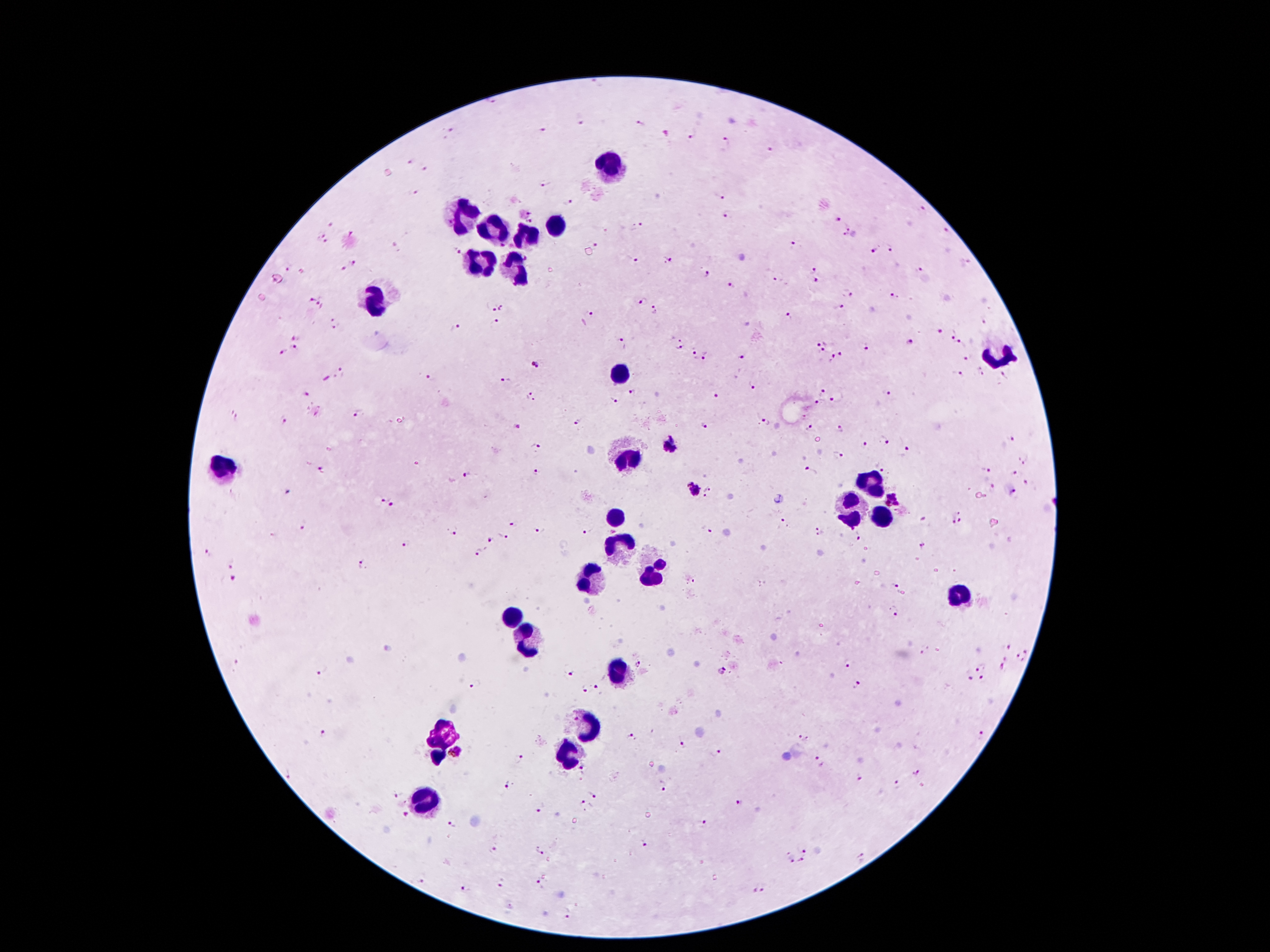

{
  "leukocyte_locations": "approximate object centers, in pixels from the top-left corner: (x=609, y=163), (x=465, y=215), (x=559, y=226), (x=493, y=229), (x=527, y=236), (x=478, y=263), (x=515, y=271), (x=375, y=292), (x=998, y=357), (x=619, y=375), (x=627, y=457), (x=223, y=466), (x=871, y=483), (x=854, y=509), (x=878, y=514), (x=615, y=521), (x=620, y=544), (x=649, y=573), (x=591, y=577), (x=962, y=593), (x=512, y=616), (x=522, y=636), (x=619, y=676), (x=587, y=726), (x=441, y=732), (x=573, y=752), (x=436, y=756), (x=425, y=805)",
  "malaria_parasite_locations": "approximate object centers, in pixels from the top-left corner: (x=492, y=102), (x=579, y=118), (x=641, y=124), (x=450, y=130), (x=541, y=132), (x=690, y=133), (x=723, y=143), (x=771, y=152), (x=410, y=162), (x=425, y=167), (x=546, y=183), (x=414, y=193), (x=720, y=195), (x=568, y=203), (x=923, y=209), (x=531, y=212), (x=727, y=213), (x=837, y=218), (x=531, y=220), (x=330, y=224), (x=637, y=226), (x=849, y=226), (x=321, y=231), (x=946, y=231), (x=351, y=233), (x=845, y=237), (x=596, y=245), (x=792, y=245), (x=326, y=246), (x=502, y=246), (x=890, y=248), (x=874, y=250), (x=458, y=251), (x=526, y=258), (x=633, y=260), (x=668, y=261), (x=353, y=263), (x=969, y=263), (x=286, y=268), (x=341, y=270), (x=812, y=270), (x=918, y=270), (x=301, y=272), (x=708, y=274), (x=778, y=279), (x=817, y=280), (x=731, y=287), (x=848, y=294), (x=894, y=296), (x=321, y=299), (x=312, y=300), (x=643, y=300), (x=837, y=307), (x=491, y=309), (x=503, y=309), (x=655, y=311), (x=592, y=315), (x=789, y=316), (x=336, y=319), (x=984, y=322), (x=495, y=324), (x=336, y=329), (x=455, y=329), (x=939, y=330), (x=954, y=334), (x=296, y=336), (x=682, y=339), (x=621, y=343), (x=817, y=344), (x=909, y=344), (x=963, y=345), (x=826, y=346), (x=679, y=347), (x=866, y=347), (x=295, y=350), (x=283, y=353), (x=841, y=354), (x=742, y=355), (x=694, y=356), (x=706, y=357), (x=969, y=357), (x=832, y=358), (x=536, y=364), (x=981, y=370), (x=341, y=371), (x=1006, y=373), (x=957, y=374), (x=430, y=377), (x=326, y=379), (x=507, y=380), (x=754, y=386), (x=821, y=391), (x=307, y=393), (x=632, y=393), (x=886, y=393), (x=717, y=395), (x=531, y=396), (x=612, y=400), (x=837, y=400), (x=819, y=402), (x=318, y=411), (x=358, y=413), (x=808, y=415), (x=238, y=418), (x=285, y=419), (x=576, y=422), (x=766, y=422), (x=703, y=426), (x=518, y=427), (x=810, y=428), (x=841, y=429), (x=1013, y=438), (x=885, y=441), (x=863, y=444), (x=536, y=446), (x=908, y=451), (x=839, y=453), (x=1024, y=460), (x=987, y=468), (x=321, y=470), (x=536, y=471), (x=810, y=472), (x=1015, y=473), (x=469, y=475), (x=687, y=482), (x=1027, y=483), (x=711, y=488), (x=992, y=489), (x=694, y=491), (x=1012, y=493), (x=703, y=495), (x=384, y=498), (x=893, y=500), (x=393, y=507), (x=956, y=509), (x=961, y=520), (x=784, y=521), (x=953, y=521), (x=924, y=522), (x=513, y=524), (x=815, y=525), (x=304, y=526), (x=706, y=529), (x=539, y=530), (x=454, y=531), (x=585, y=531), (x=502, y=535), (x=821, y=535), (x=859, y=537), (x=491, y=541), (x=405, y=543), (x=924, y=547), (x=207, y=552), (x=480, y=552), (x=232, y=564), (x=361, y=564), (x=233, y=578), (x=694, y=581), (x=895, y=586), (x=897, y=612), (x=1006, y=646), (x=1027, y=650), (x=923, y=652), (x=236, y=660), (x=1020, y=660), (x=848, y=664), (x=639, y=665), (x=1003, y=666), (x=981, y=667), (x=321, y=670), (x=569, y=671), (x=723, y=671), (x=969, y=677), (x=984, y=679), (x=475, y=683), (x=858, y=684), (x=599, y=689), (x=586, y=690), (x=324, y=734), (x=981, y=736), (x=631, y=737), (x=803, y=738), (x=683, y=745), (x=455, y=752), (x=715, y=754), (x=520, y=758), (x=818, y=762), (x=584, y=769), (x=916, y=773), (x=290, y=774), (x=857, y=779), (x=662, y=784), (x=898, y=786), (x=506, y=787), (x=401, y=793), (x=592, y=795), (x=739, y=802), (x=584, y=804), (x=542, y=806), (x=405, y=813), (x=452, y=825), (x=702, y=825), (x=643, y=845), (x=806, y=848), (x=492, y=851), (x=539, y=851), (x=865, y=858), (x=790, y=860), (x=802, y=862), (x=418, y=877), (x=503, y=884), (x=540, y=885), (x=760, y=887), (x=464, y=888)",
  "preparation": "thick blood smear",
  "stain": "Giemsa",
  "magnification": "100x",
  "patient_malaria_status": "positive for Plasmodium falciparum",
  "image_size": "1270×952 pixels",
  "capture": "smartphone camera through the microscope eyepiece",
  "field_of_view": "one from this slide"
}